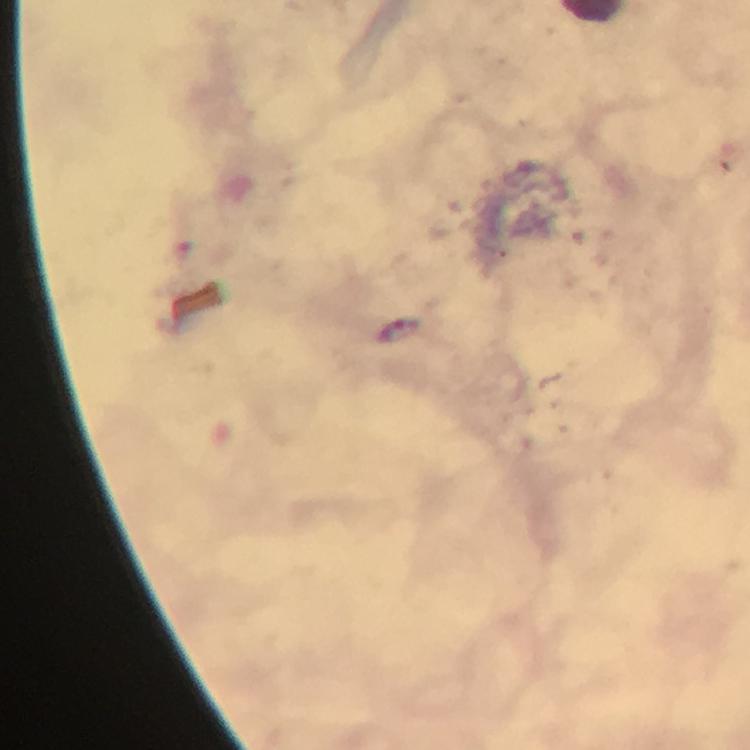

immersion oil = applied
stain = Giemsa
Plasmodium parasite locations = approximate centers as {x, y} in pixels: {387, 333}
preparation = thick blood smear
cropped from = a single field of view
magnification = 100x
context = from a malaria diagnostic workup
image size = 750×750 pixels
capture = smartphone photograph through a microscope